State which parasite is depicted.
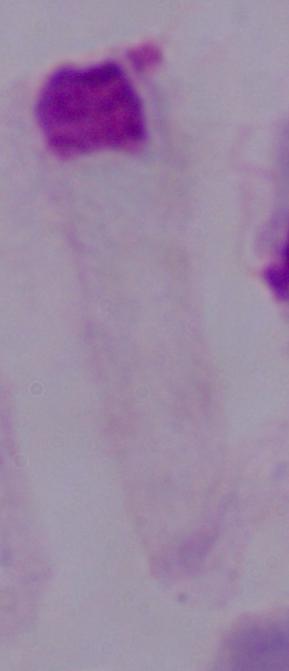

This is a trichomonad.

Summary:
  - Modality: photomicrograph
  - Magnification: 1000x